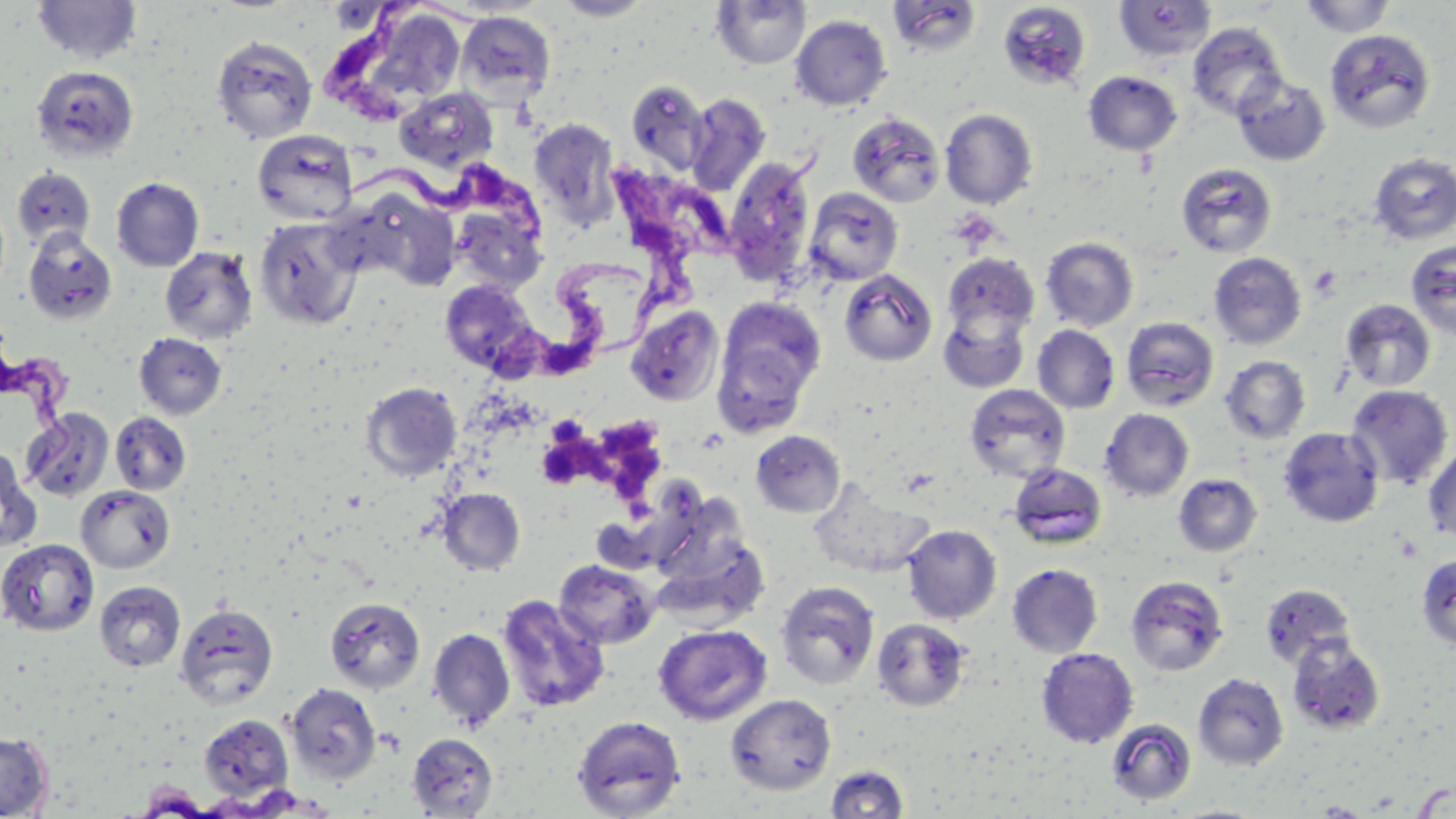

Summary:
  - Coordinate format: approximate bounding boxes as (x1, y1, x2, y2) in pixels
  - Platelet locations: (1309, 264, 1342, 299), (538, 434, 587, 491)
  - Uninfected red blood cell locations: (32, 0, 143, 64), (552, 0, 654, 20), (711, 0, 811, 69), (1114, 0, 1218, 62), (1298, 0, 1398, 37), (887, 1, 981, 56), (997, 2, 1092, 91), (326, 3, 391, 33), (456, 10, 556, 106), (791, 14, 892, 111), (375, 15, 464, 94), (1187, 23, 1287, 119), (1324, 28, 1436, 133), (211, 34, 318, 144), (31, 65, 139, 161), (1083, 71, 1181, 155), (1232, 73, 1331, 166), (626, 79, 710, 176), (394, 86, 498, 173), (685, 93, 771, 197), (940, 108, 1038, 208), (847, 112, 946, 208), (529, 118, 621, 230), (252, 129, 358, 226), (1369, 153, 1456, 244), (724, 155, 817, 288), (1176, 162, 1277, 258), (12, 167, 96, 251), (111, 176, 204, 271), (803, 187, 904, 286), (351, 188, 461, 290), (450, 203, 547, 294), (254, 216, 363, 330), (23, 229, 119, 325), (1041, 237, 1139, 331), (1405, 240, 1456, 339), (160, 247, 258, 344), (1208, 252, 1307, 350), (942, 253, 1039, 341), (839, 269, 937, 366), (439, 279, 540, 376), (717, 296, 827, 404), (1340, 299, 1436, 391), (625, 305, 725, 406), (939, 305, 1031, 393), (1121, 317, 1220, 411), (1032, 325, 1120, 413), (134, 333, 227, 420), (712, 337, 814, 438), (1221, 356, 1310, 443), (360, 381, 461, 481), (964, 384, 1070, 483), (1345, 385, 1453, 490), (1100, 408, 1194, 501), (21, 409, 114, 502), (110, 411, 191, 495), (1278, 427, 1384, 527), (751, 430, 845, 517), (1422, 442, 1456, 542), (0, 450, 41, 552), (1008, 463, 1107, 549), (1173, 474, 1262, 557), (807, 478, 934, 578), (76, 486, 175, 573), (437, 488, 525, 575), (643, 488, 753, 590), (902, 524, 1001, 623), (1, 538, 99, 636), (1416, 553, 1456, 651), (554, 559, 660, 649), (1007, 564, 1104, 657), (1126, 575, 1229, 676), (94, 580, 186, 672), (774, 580, 880, 690), (1260, 584, 1355, 668), (496, 594, 610, 713), (324, 597, 425, 693), (175, 602, 279, 709), (871, 618, 972, 711), (654, 624, 772, 726), (427, 628, 516, 731), (1286, 636, 1387, 734), (1036, 648, 1139, 748), (1193, 673, 1288, 770), (285, 683, 382, 784), (725, 693, 836, 795), (198, 714, 294, 801), (572, 715, 686, 819), (1106, 718, 1197, 806), (0, 732, 54, 818), (407, 732, 498, 817), (825, 764, 909, 818)
  - Trypanosoma brucei locations: (331, 0, 417, 125), (350, 155, 555, 238), (618, 165, 717, 355), (497, 262, 656, 379), (4, 348, 95, 486)
  - Slide-level diagnosis: Trypanosoma brucei
  - Image size: 1456×819 pixels
  - Stain: May-Grünwald-Giemsa
  - Modality: light microscopy
  - Magnification: 1000x
  - Field of view: single
  - Preparation: thin blood smear